Comment on the morphology of the erythrocytes.
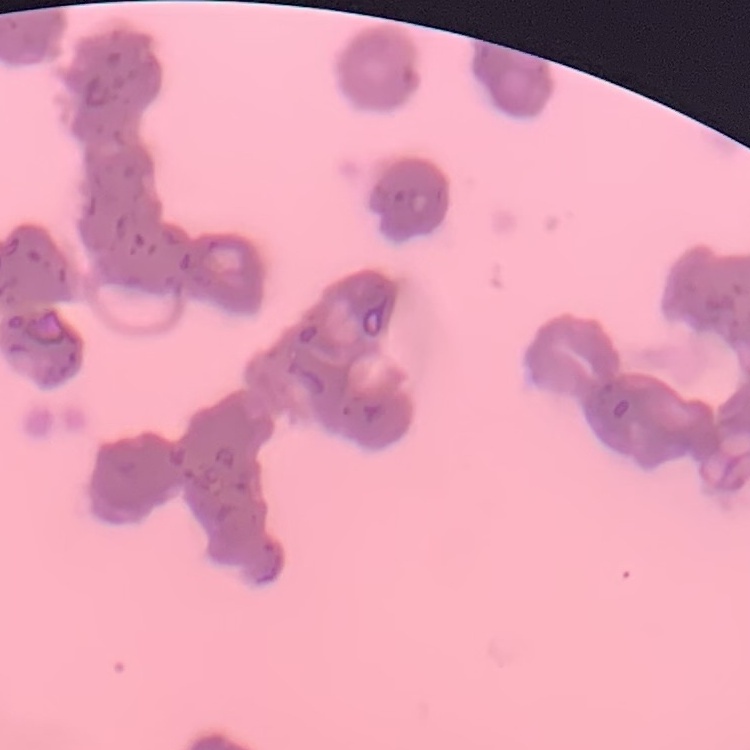
Rouleaux formation.

Summary:
  - Image type: square crop of a larger photomicrograph
  - Stain: Field's or Giemsa
  - Preparation: thin peripheral smear